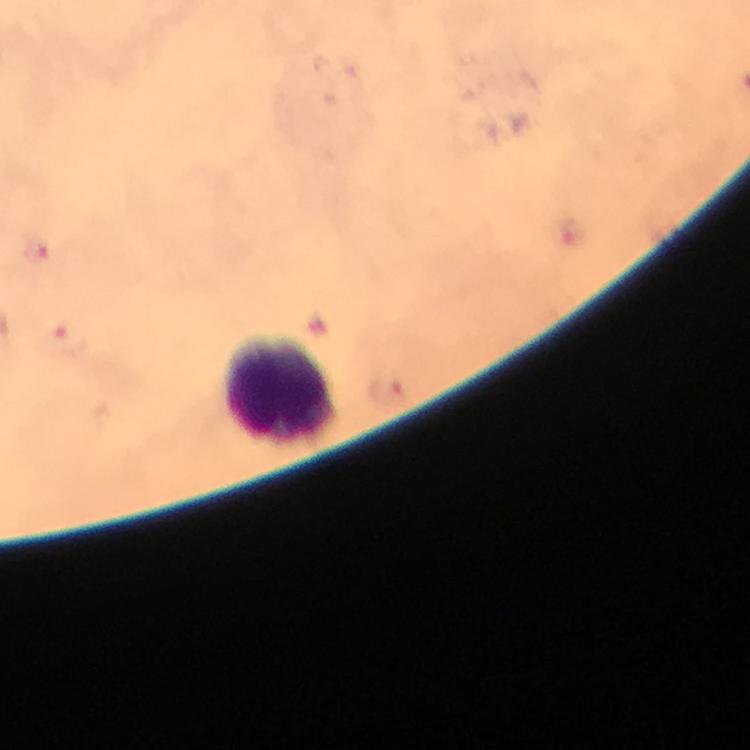

Approximate centers as {x, y} in pixels.
Summary:
  - Leukocyte locations: {282, 389}
  - Malaria parasite locations: {572, 230}, {37, 249}, {67, 338}, {387, 390}
  - Magnification: 100x
  - Cropped from: a single field of view
  - Preparation: thick smear
  - Image size: 750×750 pixels
  - Immersion oil: used
  - Capture: smartphone photograph through a microscope
  - Stain: Giemsa
  - Context: from a diagnostic examination for malaria